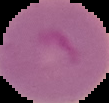
The area outside the segmented cell region is set to black. From a thin blood smear. Malaria status: parasitized. Image is 109×103 pixels.